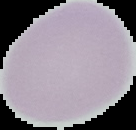

preparation = thin blood film
malaria status = uninfected
image type = segmented cell region with the area outside set to black
image size = 136×130 pixels